Name the blood parasite species.
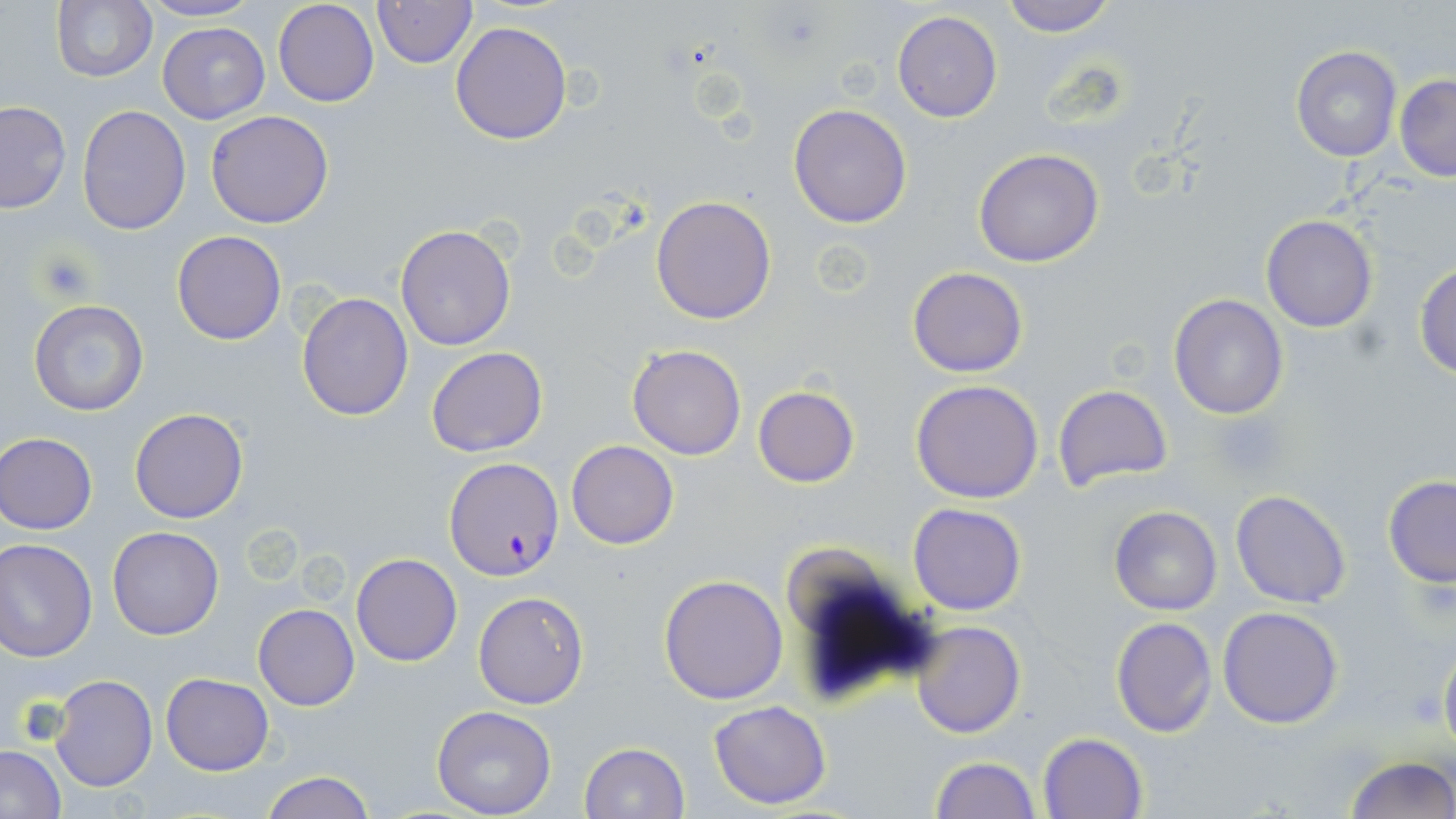

Plasmodium falciparum.

Summary:
  - Coordinate format: approximate bounding boxes as [x1, y1, x2, y2] in pixels
  - Uninfected red blood cell locations: [51, 0, 158, 86], [139, 0, 262, 23], [273, 0, 380, 107], [999, 0, 1118, 37], [372, 1, 477, 70], [892, 11, 1002, 122], [450, 20, 573, 144], [156, 21, 271, 124], [1291, 46, 1401, 162], [1394, 74, 1456, 182], [0, 101, 73, 214], [788, 103, 911, 227], [76, 105, 192, 234], [205, 110, 334, 228], [973, 147, 1105, 267], [650, 195, 777, 323], [1260, 215, 1378, 332], [394, 224, 518, 351], [172, 231, 287, 344], [1413, 261, 1456, 380], [908, 267, 1027, 378], [297, 292, 414, 422], [1168, 294, 1289, 420], [28, 299, 150, 418], [626, 345, 746, 460], [427, 347, 546, 457], [910, 379, 1044, 503], [1052, 384, 1175, 496], [753, 385, 860, 487], [129, 407, 248, 524], [0, 432, 98, 534], [567, 440, 678, 549], [1382, 475, 1456, 587], [1230, 490, 1353, 608], [908, 503, 1027, 614], [1109, 505, 1221, 615], [107, 528, 224, 640], [0, 538, 96, 661], [780, 547, 893, 643], [351, 553, 461, 666], [658, 573, 788, 704], [473, 591, 589, 709], [254, 604, 359, 710], [1217, 606, 1344, 730], [1109, 616, 1217, 737], [911, 621, 1025, 738], [1438, 640, 1456, 756], [161, 673, 273, 775], [49, 675, 157, 791], [706, 700, 833, 808], [431, 706, 559, 818], [1038, 732, 1147, 819], [577, 742, 689, 819], [0, 746, 66, 819], [1343, 755, 1454, 819], [929, 756, 1040, 819], [258, 770, 379, 819]
  - Platelet locations: [36, 251, 97, 302], [1213, 417, 1284, 478]
  - Plasmodium falciparum-infected red blood cell locations: [445, 457, 563, 579]
  - Stain: May-Grünwald-Giemsa
  - Magnification: 1000x
  - Image size: 1456×819 pixels
  - Modality: light microscopy
  - Field of view: single
  - Preparation: thin blood film